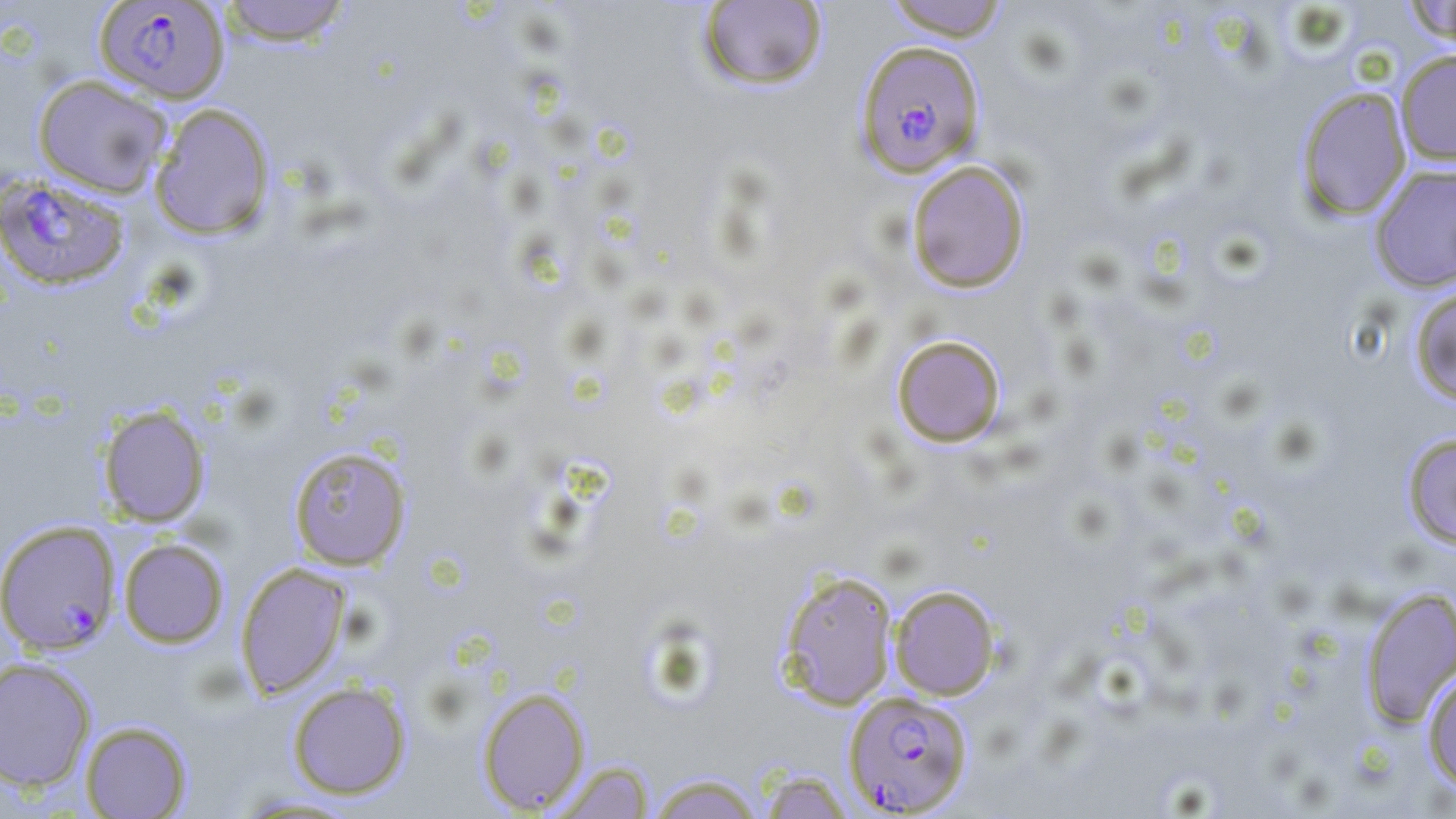
Summary:
  - Coordinate format: approximate bounding boxes as [x1, y1, x2, y2] in pixels
  - Plasmodium falciparum-infected red blood cell locations: [94, 1, 230, 103], [854, 39, 986, 178], [0, 175, 130, 291], [0, 520, 121, 656], [842, 689, 975, 815]
  - Uninfected red blood cell locations: [218, 0, 354, 46], [881, 0, 1012, 41], [1399, 0, 1456, 46], [696, 1, 829, 91], [1395, 50, 1456, 165], [33, 74, 172, 197], [1295, 86, 1412, 221], [149, 102, 276, 240], [906, 160, 1030, 293], [1368, 164, 1456, 293], [1409, 284, 1456, 406], [891, 334, 1007, 448], [97, 403, 212, 526], [1401, 431, 1456, 551], [288, 445, 413, 570], [118, 538, 230, 648], [234, 562, 352, 700], [777, 569, 899, 710], [889, 584, 1001, 700], [1360, 585, 1456, 729], [0, 657, 97, 792], [1421, 668, 1456, 795], [287, 680, 412, 799], [476, 687, 590, 814], [80, 720, 193, 818], [548, 759, 656, 819], [754, 768, 858, 818], [644, 771, 768, 818], [230, 792, 368, 817]
  - Slide-level diagnosis: Plasmodium falciparum
  - Modality: optical microscopy
  - Stain: May-Grünwald-Giemsa
  - Magnification: 1000x
  - Preparation: thin blood film
  - Image size: 1456×819 pixels
  - Field of view: one of a larger specimen